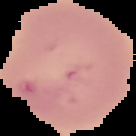
result = no Plasmodium parasites detected
image size = 136×136 pixels
image type = segmented cell region on a black background
preparation = thin blood smear